Give the position of every malaria parasite.
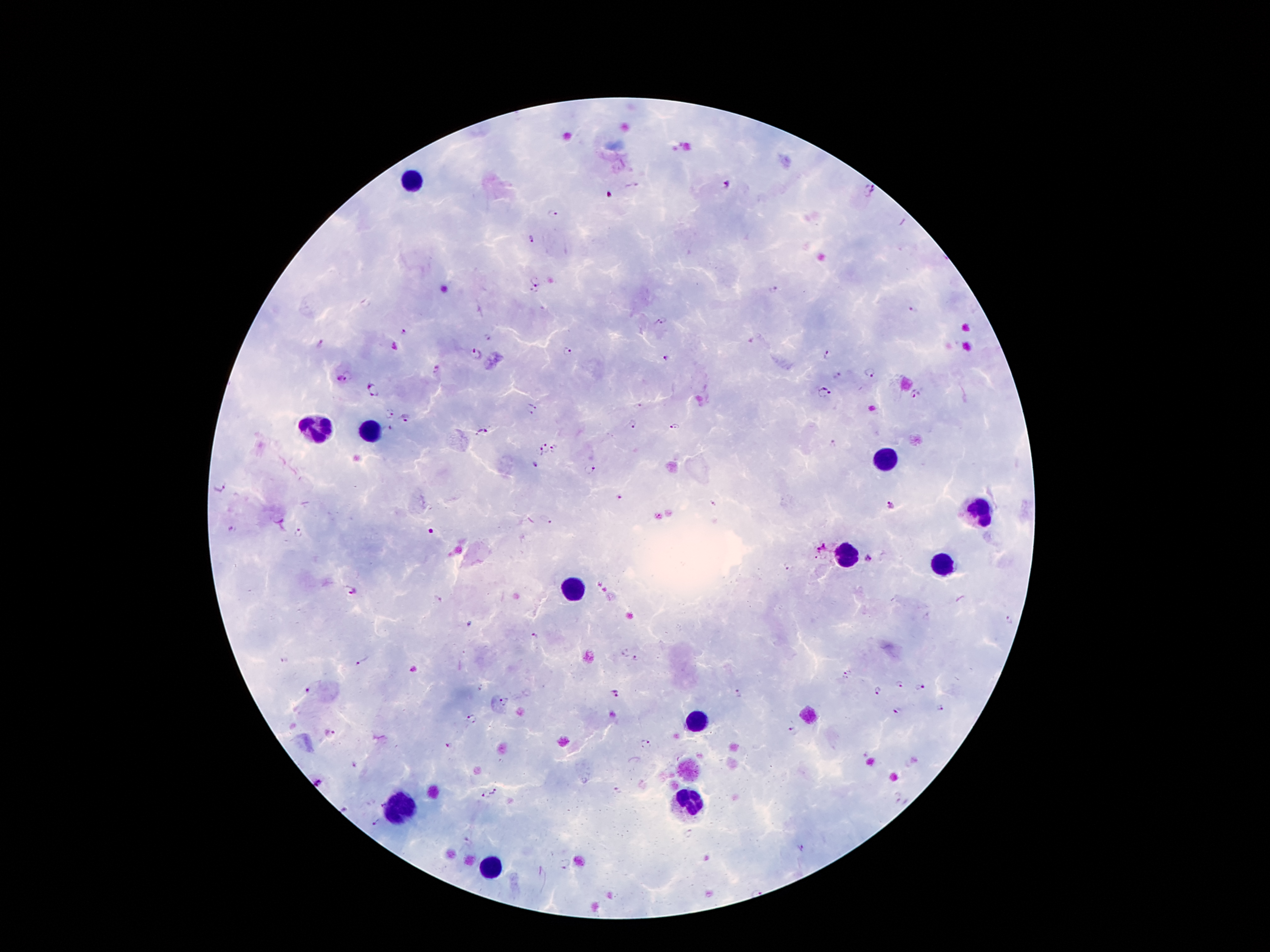
Approximate centers as [x, y] in pixels.
Malaria parasites: [724, 186], [871, 189], [611, 194], [552, 215], [532, 238], [537, 277], [773, 291], [532, 292], [914, 308], [662, 323], [406, 333], [488, 338], [320, 344], [476, 353], [568, 353], [826, 354], [666, 357], [437, 369], [870, 373], [346, 375], [372, 389], [824, 390], [918, 395], [533, 404], [638, 407], [387, 413], [526, 414], [407, 419], [632, 423], [673, 426], [386, 428], [481, 431], [545, 446], [833, 446], [554, 447], [539, 451], [536, 464], [590, 469], [219, 486], [619, 497], [712, 503], [891, 506], [545, 521], [233, 529], [432, 532], [299, 533], [823, 549], [870, 559], [787, 567], [353, 592], [437, 600], [1010, 621], [536, 638], [636, 659], [285, 660], [362, 662], [847, 675], [900, 684], [921, 687], [875, 690], [307, 691], [739, 693], [617, 694], [505, 702], [939, 709], [897, 711], [469, 715], [476, 722], [791, 731], [330, 735], [647, 744], [449, 745], [495, 791], [619, 791], [485, 795], [897, 798], [380, 805], [376, 823], [468, 843], [800, 849], [564, 863].

{
  "magnification": "100x",
  "image_size": "1270×952 pixels",
  "stain": "Giemsa",
  "leukocyte_locations": "approximate centers as [x, y] in pixels: [410, 179], [318, 431], [370, 433], [887, 460], [979, 511], [847, 554], [943, 564], [574, 589], [700, 721], [691, 805], [400, 806], [490, 867]",
  "field_of_view": "single",
  "capture": "smartphone through the microscope eyepiece",
  "patient_malaria_status": "infected with Plasmodium falciparum",
  "preparation": "thick peripheral-blood smear"
}